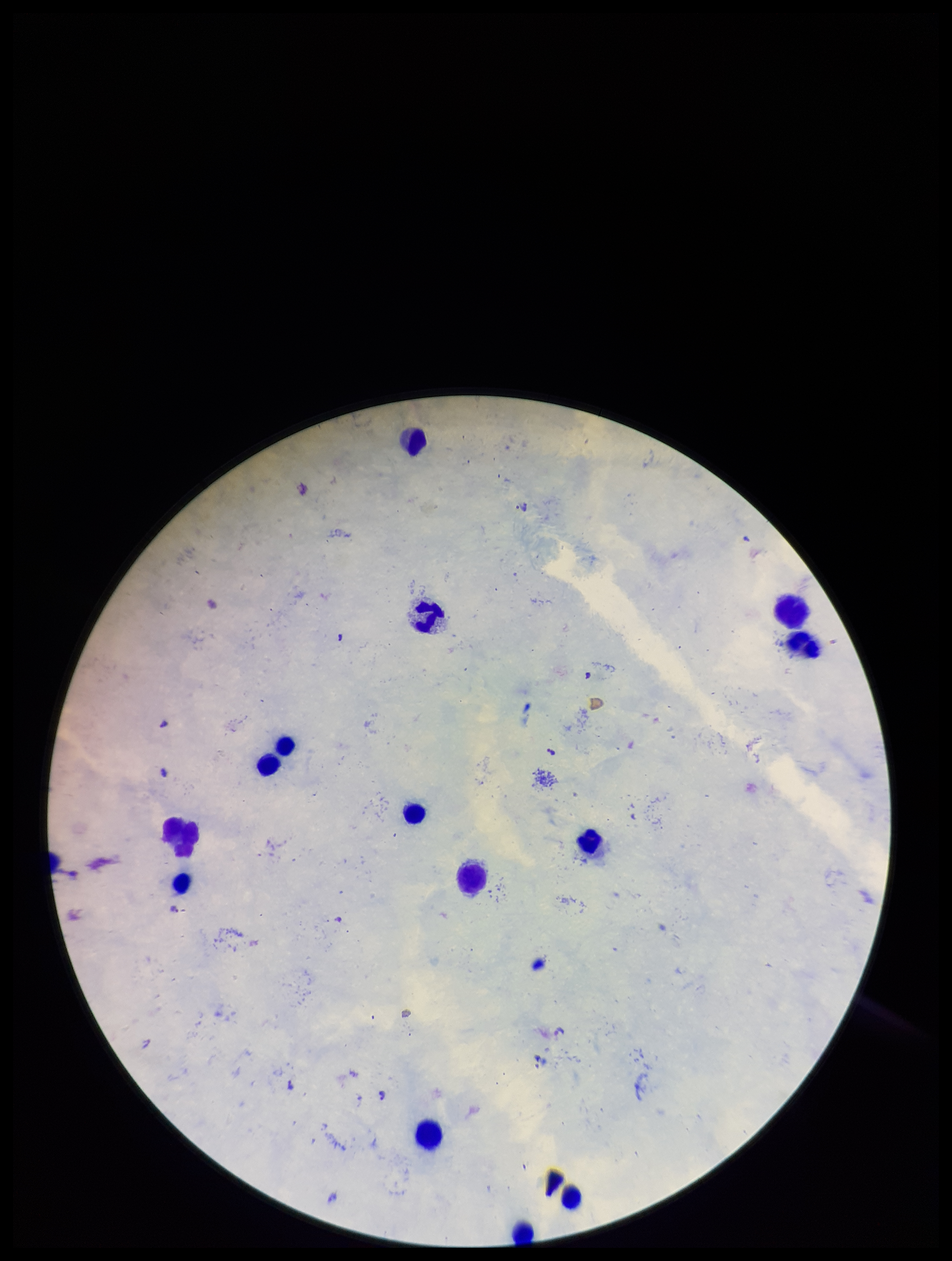

preparation = thick
image size = 952×1261 pixels
field of view = single
patient malaria status = infected
leukocyte count = 14
capture = smartphone photograph through the microscope eyepiece
stain = Giemsa
parasite count = 6
species reported for this patient = Plasmodium falciparum
Plasmodium parasites = seen